Name the parasite shown.
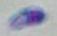

This is Toxoplasma gondii.

Summary:
  - Magnification: 1000x
  - Modality: photomicrograph